Locate and identify every blood parasite.
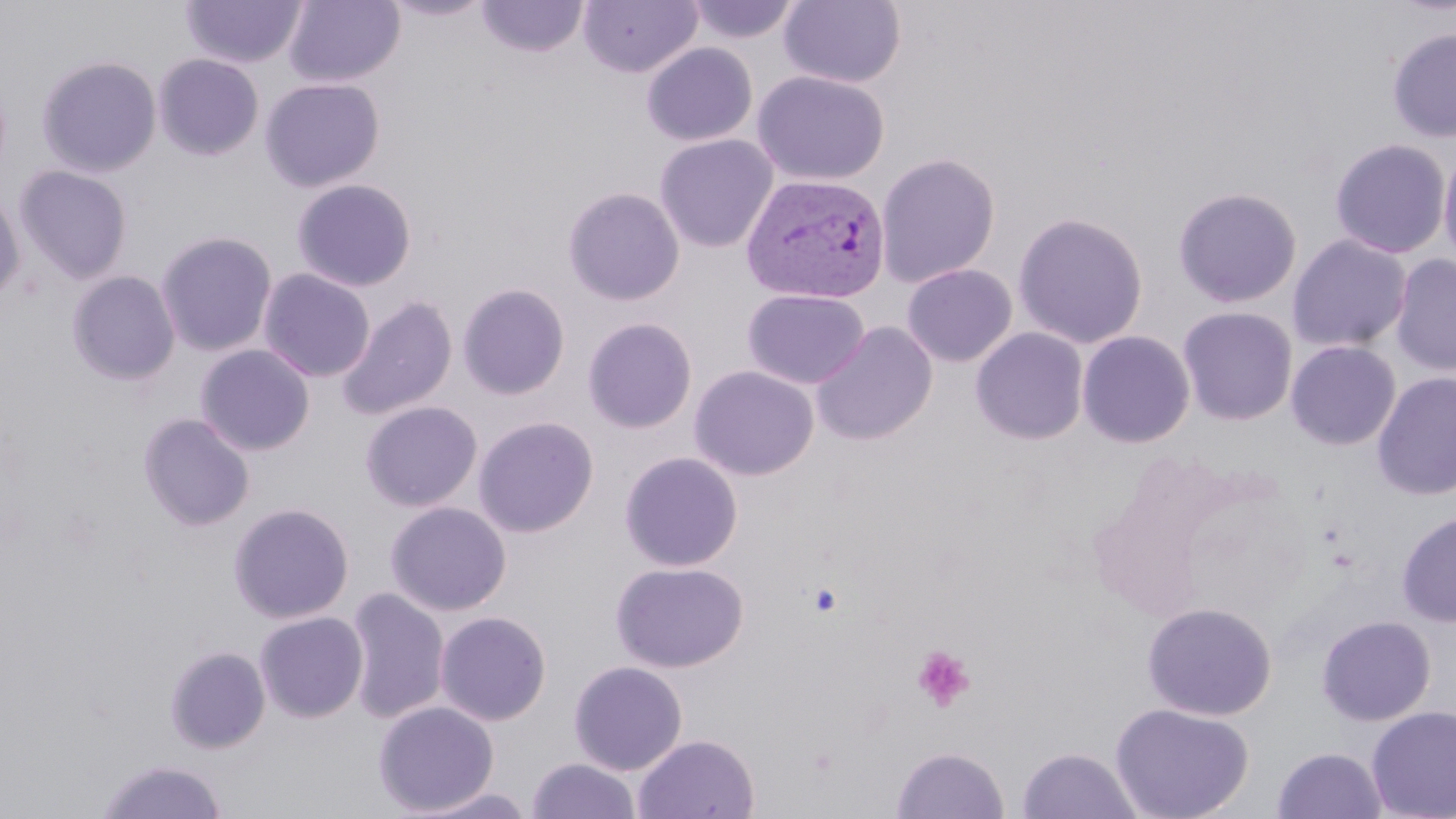
Approximate bounding boxes as [x1, y1, x2, y2] in pixels.
Plasmodium vivax-infected red blood cells: [741, 173, 891, 304].
No Plasmodium falciparum, Plasmodium ovale, Plasmodium malariae, Babesia divergens, or Trypanosoma brucei observed.

{
  "slide_level_diagnosis": "Plasmodium vivax",
  "modality": "optical microscopy",
  "field_of_view": "single",
  "magnification": "1000x",
  "preparation": "thin blood smear",
  "stain": "May-Grünwald-Giemsa",
  "platelet_locations": "approximate bounding boxes as [x1, y1, x2, y2] in pixels: [807, 581, 844, 618], [912, 645, 976, 713]",
  "uninfected_red_blood_cell_locations": "approximate bounding boxes as [x1, y1, x2, y2] in pixels: [284, 0, 405, 87], [381, 0, 495, 21], [684, 0, 804, 43], [181, 1, 308, 68], [477, 1, 589, 58], [578, 1, 702, 78], [779, 1, 906, 88], [1387, 27, 1456, 143], [641, 43, 758, 146], [153, 54, 264, 160], [37, 55, 161, 177], [752, 70, 890, 186], [260, 77, 385, 192], [654, 134, 778, 253], [1328, 137, 1452, 259], [1438, 140, 1456, 271], [875, 153, 1001, 287], [14, 165, 133, 283], [291, 178, 417, 292], [1172, 186, 1302, 308], [0, 187, 26, 303], [562, 187, 685, 305], [1012, 210, 1149, 348], [156, 231, 278, 356], [1287, 233, 1413, 353], [1390, 252, 1456, 376], [901, 263, 1017, 367], [258, 269, 376, 382], [67, 271, 180, 386], [457, 283, 570, 400], [742, 288, 870, 389], [336, 295, 458, 420], [1177, 306, 1298, 426], [583, 317, 698, 433], [810, 322, 938, 445], [970, 326, 1089, 445], [1076, 330, 1195, 448], [1285, 339, 1402, 451], [195, 344, 315, 456], [689, 365, 819, 481], [1372, 370, 1456, 501], [360, 401, 482, 511], [138, 412, 255, 532], [473, 416, 598, 537], [619, 451, 743, 572], [385, 501, 511, 616], [228, 502, 355, 624], [1396, 511, 1456, 628], [610, 561, 748, 672], [344, 587, 450, 724], [1142, 601, 1277, 721], [255, 610, 369, 723], [435, 611, 552, 726], [1316, 614, 1437, 726], [163, 636, 370, 743], [165, 645, 271, 754], [568, 661, 688, 775], [374, 701, 499, 815], [1110, 702, 1254, 819], [1367, 706, 1456, 819], [633, 733, 760, 819], [891, 746, 1010, 819], [1016, 747, 1143, 819], [1273, 747, 1387, 819], [526, 757, 641, 818], [95, 759, 227, 819], [413, 787, 537, 819]",
  "image_size": "1456×819 pixels"
}